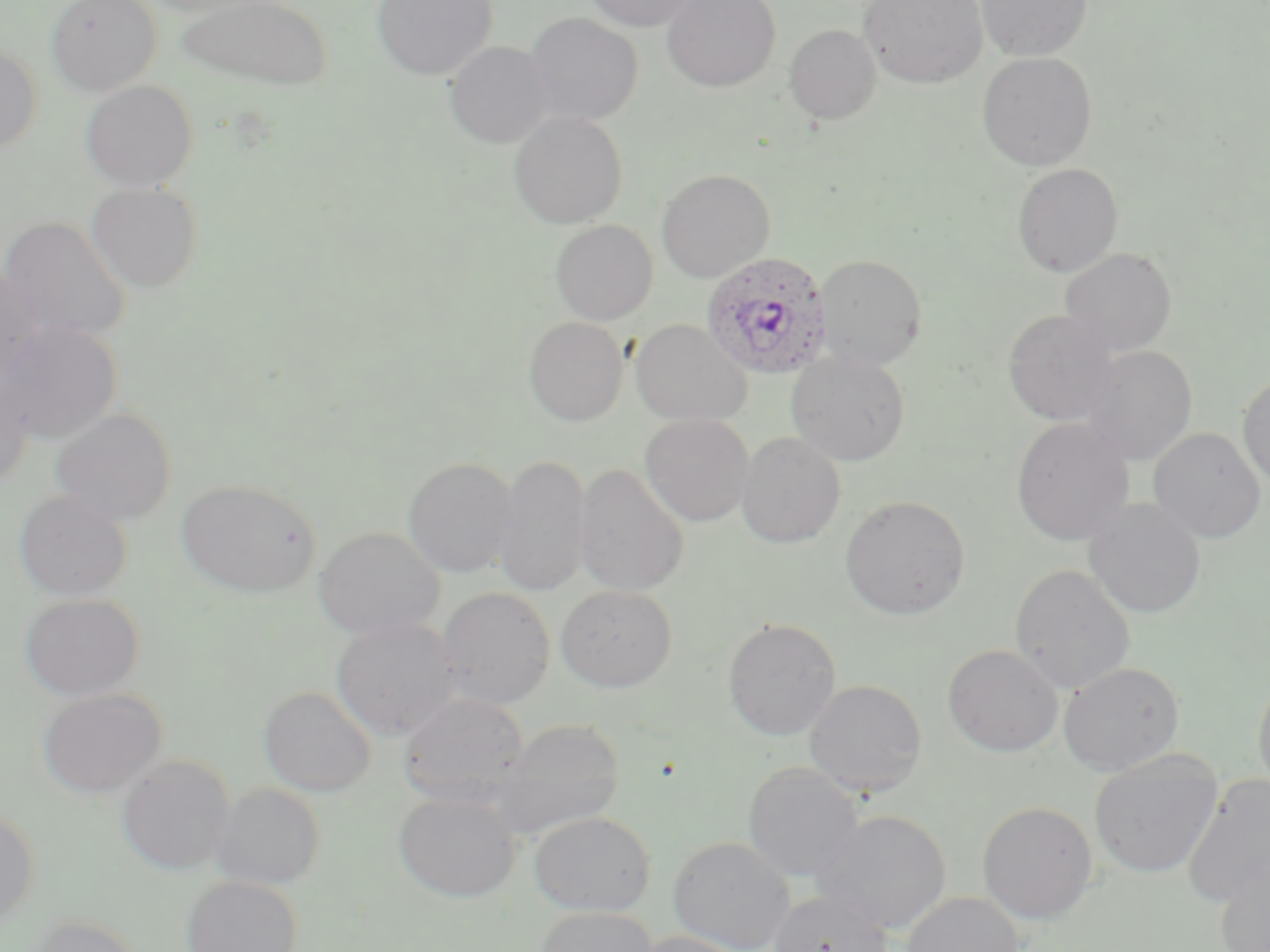

{
  "slide_level_diagnosis": "Plasmodium ovale",
  "field_of_view": "single",
  "preparation": "thin blood film",
  "modality": "light microscopy",
  "image_size": "1270×952 pixels",
  "stain": "May-Grünwald-Giemsa",
  "magnification": "1000x",
  "uninfected_red_blood_cell_locations": "approximate bounding boxes as (x1,y1)-(x2,y2) corner pairs in pixels: (46,0)-(162,95), (134,0)-(268,17), (177,0)-(332,90), (372,0)-(498,81), (582,0)-(701,31), (662,0)-(780,92), (859,0)-(987,88), (975,0)-(1093,62), (525,12)-(643,125), (784,24)-(881,125), (445,41)-(554,148), (0,44)-(42,156), (978,52)-(1097,170), (80,80)-(199,191), (509,111)-(628,229), (1012,163)-(1123,277), (656,168)-(775,282), (86,182)-(203,292), (0,216)-(132,344), (550,220)-(658,324), (1060,247)-(1177,356), (814,254)-(928,371), (0,267)-(46,384), (1003,308)-(1120,425), (523,317)-(629,426), (630,319)-(751,426), (0,322)-(121,443), (1082,345)-(1197,465), (787,350)-(910,467), (0,372)-(32,489), (1238,372)-(1270,489), (49,406)-(177,525), (639,414)-(754,526), (1011,417)-(1135,547), (1148,427)-(1266,543), (736,431)-(846,548), (494,454)-(591,598), (403,456)-(519,577), (573,464)-(689,596), (177,479)-(320,598), (14,489)-(132,601), (840,495)-(970,620), (1083,498)-(1207,619), (313,526)-(445,639), (1010,564)-(1135,694), (556,584)-(677,691), (437,586)-(555,709), (19,593)-(145,700), (330,616)-(460,740), (723,617)-(842,741), (943,643)-(1063,757), (1059,662)-(1184,775), (1253,671)-(1270,801), (804,679)-(927,798), (258,686)-(377,796), (36,688)-(168,798), (399,691)-(529,806), (492,718)-(625,839), (1089,751)-(1223,878), (117,755)-(235,875), (742,762)-(865,882), (1181,774)-(1270,908), (210,782)-(325,890), (393,788)-(522,902), (977,800)-(1098,923), (0,808)-(39,926), (812,810)-(951,934), (529,811)-(656,915), (668,836)-(796,952), (1215,862)-(1270,952), (181,875)-(302,952), (767,889)-(894,952), (901,892)-(1024,952), (536,906)-(658,952), (23,914)-(145,952), (630,931)-(751,952)",
  "plasmodium_ovale_infected_red_blood_cell_locations": "approximate bounding boxes as (x1,y1)-(x2,y2) corner pairs in pixels: (701,252)-(833,380)"
}